Assess this cell for malaria.
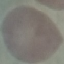
Uninfected.

stain: Giemsa
capture: smartphone camera at the microscope eyepiece
image_type: cell patch, automatically extracted from a larger field of view and resized to 64 × 64 pixels
preparation: thin blood smear